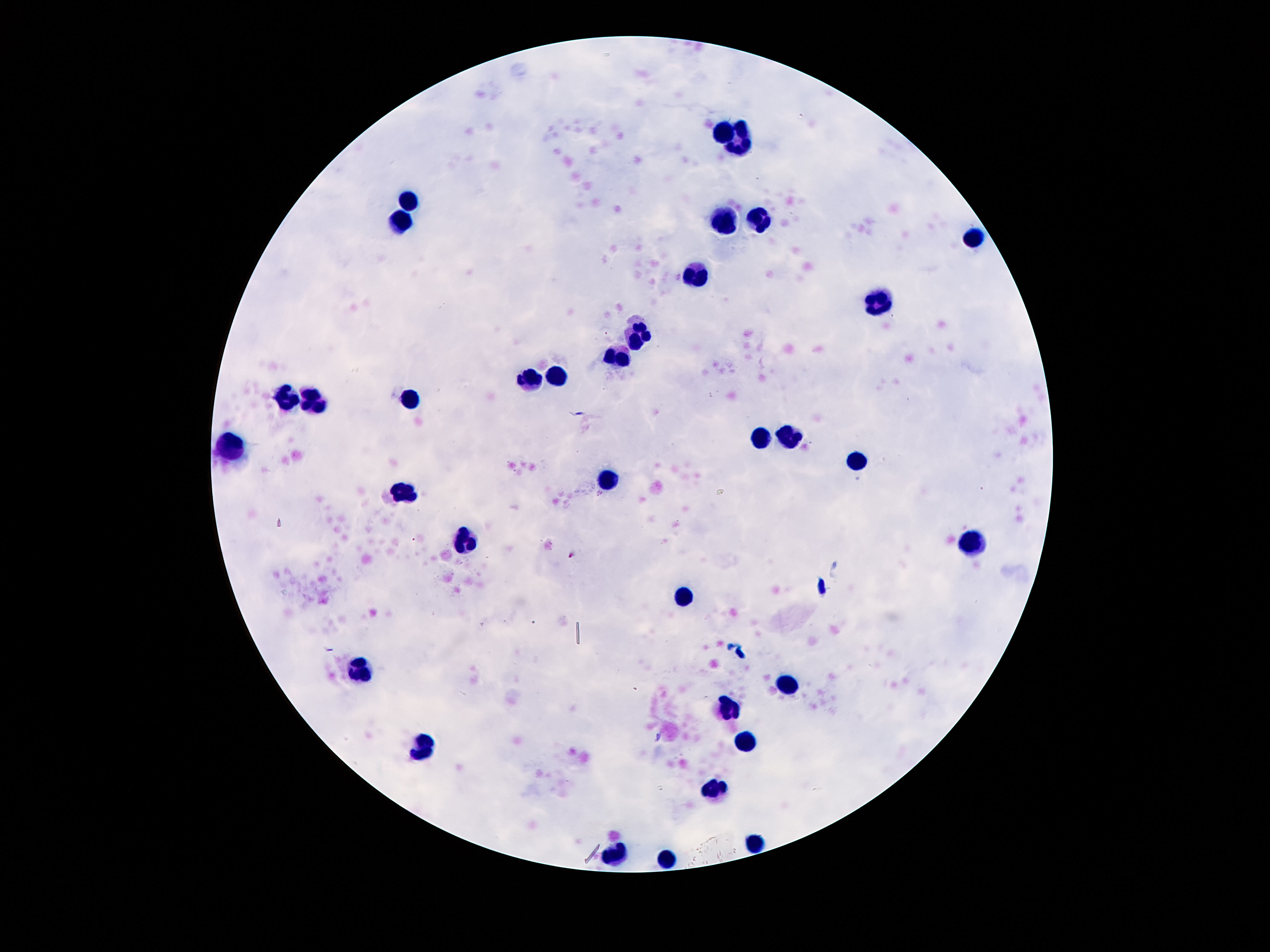
{
  "leukocyte_locations": "approximate centers as [x, y] in pixels: [722, 130], [741, 144], [407, 203], [402, 221], [760, 221], [722, 226], [972, 236], [697, 275], [880, 301], [640, 333], [620, 358], [528, 379], [557, 379], [288, 397], [410, 398], [319, 401], [764, 436], [792, 436], [232, 447], [853, 463], [608, 485], [407, 492], [969, 542], [466, 544], [685, 594], [361, 671], [792, 687], [731, 710], [746, 741], [423, 748], [717, 789], [753, 843], [615, 855], [668, 857]",
  "image_size": "1270×952 pixels",
  "stain": "Giemsa",
  "magnification": "100x",
  "patient_malaria_status": "not infected",
  "field_of_view": "single",
  "preparation": "thick blood film",
  "capture": "smartphone camera through the microscope eyepiece"
}